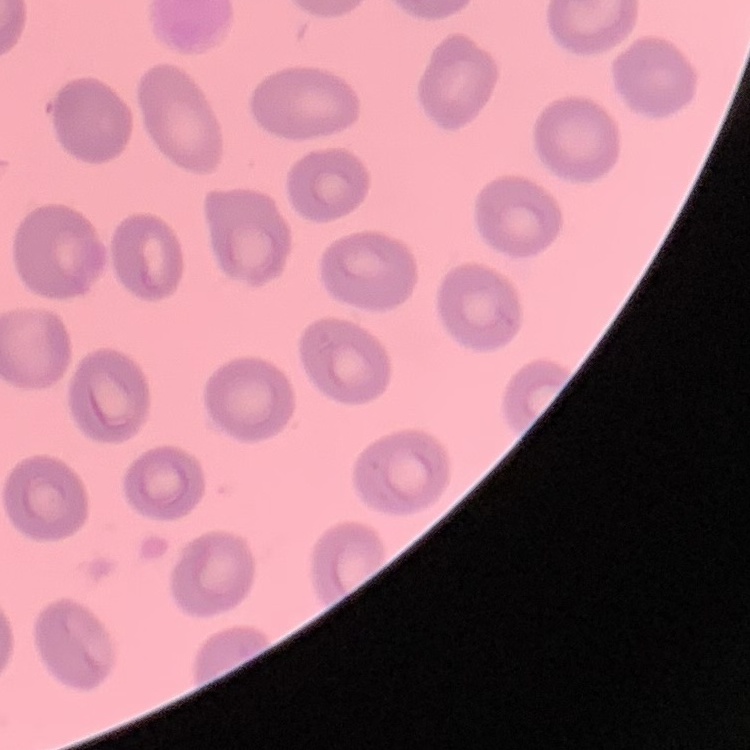

{
  "erythrocyte_morphology": "no rouleaux formation",
  "image_type": "one tile cut from a larger photomicrograph",
  "stain": "Field's or Giemsa",
  "preparation": "thin peripheral smear"
}